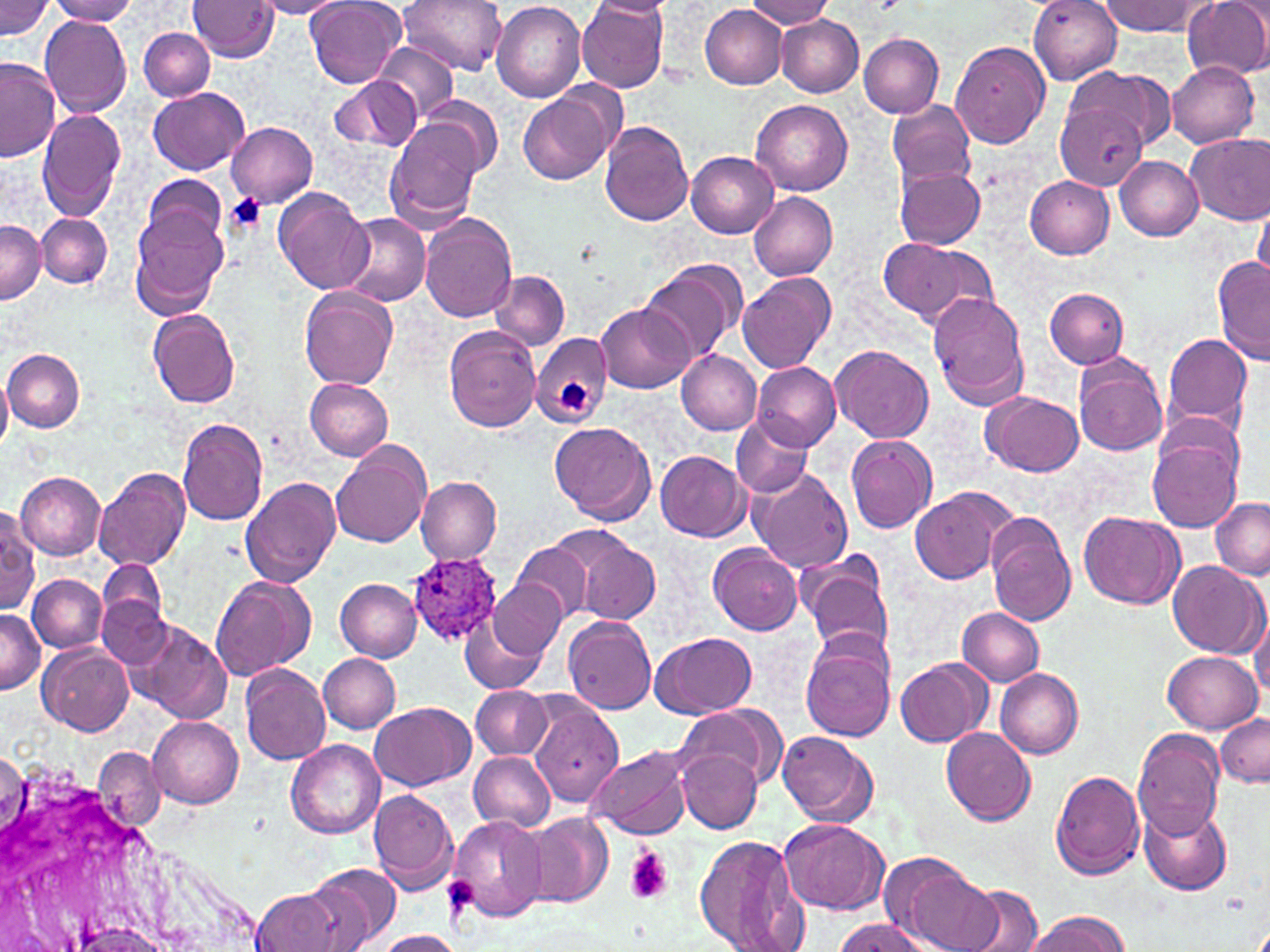

Approximate bounding boxes as (x1,y1)-(x2,y2) corner pairs in pixels. Plasmodium ovale-infected red blood cell locations: (406,552)-(500,646). Platelet locations: (225,193)-(266,234), (554,375)-(592,415), (624,847)-(672,905). Uninfected red blood cell locations: (44,0)-(140,24), (306,0)-(405,88), (399,0)-(505,75), (579,0)-(671,93), (592,0)-(674,19), (744,0)-(835,29), (1028,0)-(1122,84), (1183,0)-(1270,79), (0,1)-(54,39), (187,1)-(279,62), (251,1)-(348,19), (491,1)-(586,103), (1098,1)-(1207,35), (699,3)-(787,87), (40,15)-(133,117), (777,17)-(863,97), (139,28)-(215,100), (858,33)-(943,118), (373,41)-(457,124), (950,42)-(1050,148), (0,58)-(60,163), (1166,61)-(1259,148), (1063,68)-(1175,155), (329,76)-(421,154), (147,88)-(251,176), (519,91)-(616,185), (418,98)-(503,174), (886,99)-(976,192), (751,100)-(852,195), (1054,102)-(1153,190), (37,109)-(126,221), (386,120)-(485,227), (598,121)-(692,226), (227,122)-(318,205), (1185,134)-(1270,223), (687,152)-(778,239), (1114,155)-(1203,241), (895,166)-(985,250), (141,173)-(229,260), (1025,176)-(1114,259), (272,189)-(373,297), (749,192)-(838,280), (1253,202)-(1270,283), (128,207)-(230,320), (339,212)-(431,306), (37,213)-(112,289), (419,213)-(516,322), (1,219)-(43,304), (876,240)-(996,330), (1213,257)-(1270,366), (640,261)-(743,367), (491,270)-(570,349), (737,271)-(837,374), (300,287)-(398,389), (1045,287)-(1129,368), (927,291)-(1029,410), (595,302)-(695,393), (148,308)-(243,408), (444,327)-(542,432), (530,331)-(612,428), (1159,331)-(1253,433), (832,344)-(933,442), (2,349)-(86,433), (676,350)-(761,435), (1072,351)-(1169,458), (753,362)-(840,449), (1,374)-(13,452), (305,379)-(394,460), (985,392)-(1083,477), (731,414)-(812,499), (175,418)-(270,525), (549,422)-(655,523), (845,435)-(938,534), (1146,436)-(1242,533), (331,442)-(431,546), (656,451)-(750,542), (95,467)-(191,570), (749,467)-(853,572), (14,471)-(107,560), (416,475)-(501,562), (240,476)-(342,587), (909,485)-(1017,586), (1210,497)-(1270,578), (1078,509)-(1184,609), (0,513)-(39,614), (986,516)-(1077,626), (567,537)-(660,625), (513,539)-(597,623), (708,545)-(802,636), (800,556)-(894,656), (97,559)-(166,637), (1167,560)-(1266,658), (28,575)-(106,652), (209,576)-(314,681), (336,578)-(421,661), (490,580)-(567,658), (97,595)-(174,670), (957,607)-(1044,685), (0,609)-(43,695), (1250,610)-(1270,701), (461,612)-(547,695), (563,615)-(657,713), (131,621)-(231,723), (651,632)-(757,718), (800,636)-(896,741), (38,643)-(135,735), (1162,650)-(1261,732), (319,654)-(400,733), (895,658)-(990,747), (240,664)-(332,764), (993,666)-(1082,759), (470,686)-(551,760), (529,693)-(625,809), (369,702)-(475,791), (675,705)-(786,794), (1215,714)-(1269,786), (147,715)-(243,807), (941,727)-(1036,826), (1132,729)-(1226,840), (778,731)-(879,827), (288,741)-(384,838), (94,746)-(165,831), (584,746)-(693,841), (677,749)-(763,833), (469,750)-(557,833), (1,752)-(26,840), (1049,769)-(1146,879), (368,788)-(459,892), (1141,805)-(1233,895), (525,812)-(615,908), (450,815)-(547,922), (775,817)-(889,915), (693,833)-(810,952), (875,852)-(993,949), (305,862)-(400,950), (958,885)-(1046,952), (249,887)-(344,952), (1026,911)-(1130,952), (831,919)-(931,952), (71,922)-(175,952), (375,931)-(461,952). White blood cell locations: (0,758)-(277,952). Slide-level diagnosis: Plasmodium ovale. One field of a larger specimen. 1000x magnification. May-Grünwald-Giemsa stain. Image is 1270×952 pixels. Optical microscopy. Thin blood film.